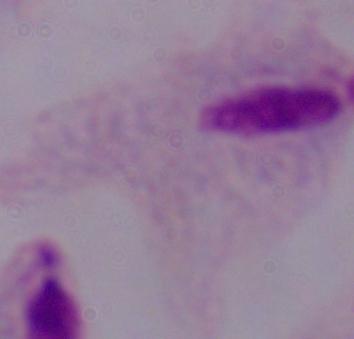
A trichomonad is shown. Photomicrograph. 1000x magnification.